Classify this cell by malaria status.
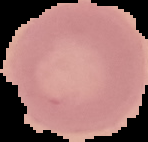

Uninfected.

From a thin blood smear. Image is 148×142 pixels. Cell region segmented out of the field of view; the surrounding area is masked to black.